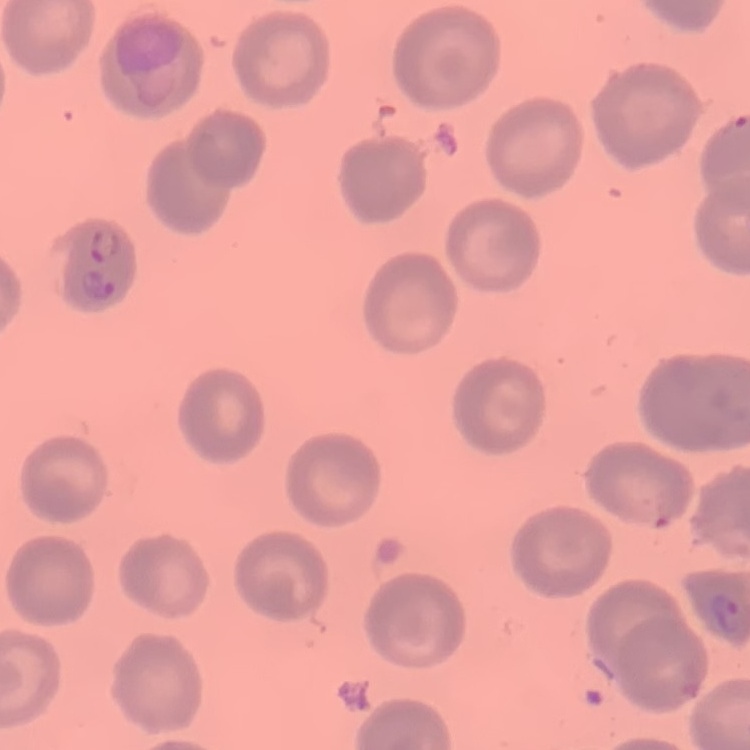
erythrocyte morphology = no rouleaux formation
image type = one tile cut from a larger photomicrograph
preparation = thin blood film
stain = Field's or Giemsa